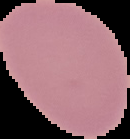
Summary:
  - Result: no malaria parasites seen
  - Image size: 130×139 pixels
  - Preparation: thin blood smear
  - Image type: segmented cell region with the area outside set to black